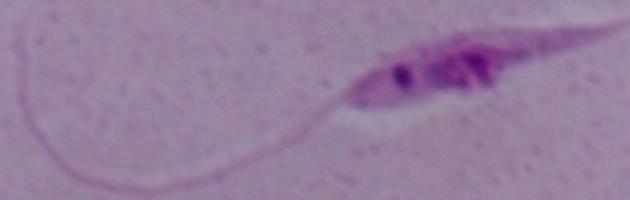
{
  "magnification": "1000x",
  "modality": "micrograph",
  "identification": "Leishmania"
}